State which parasite is depicted.
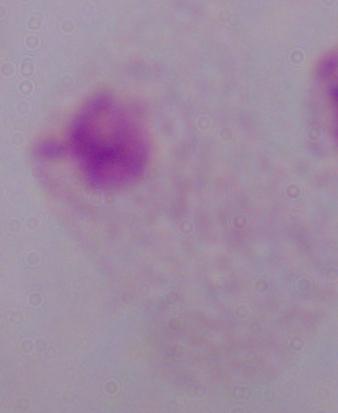
This is a trichomonad.

magnification = 1000x
modality = photomicrograph